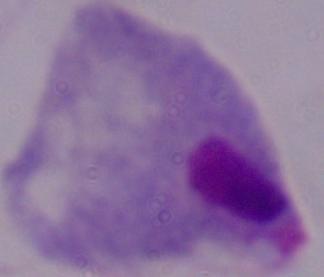 Photomicrograph. A trichomonad is shown. Captured at 1000x magnification.